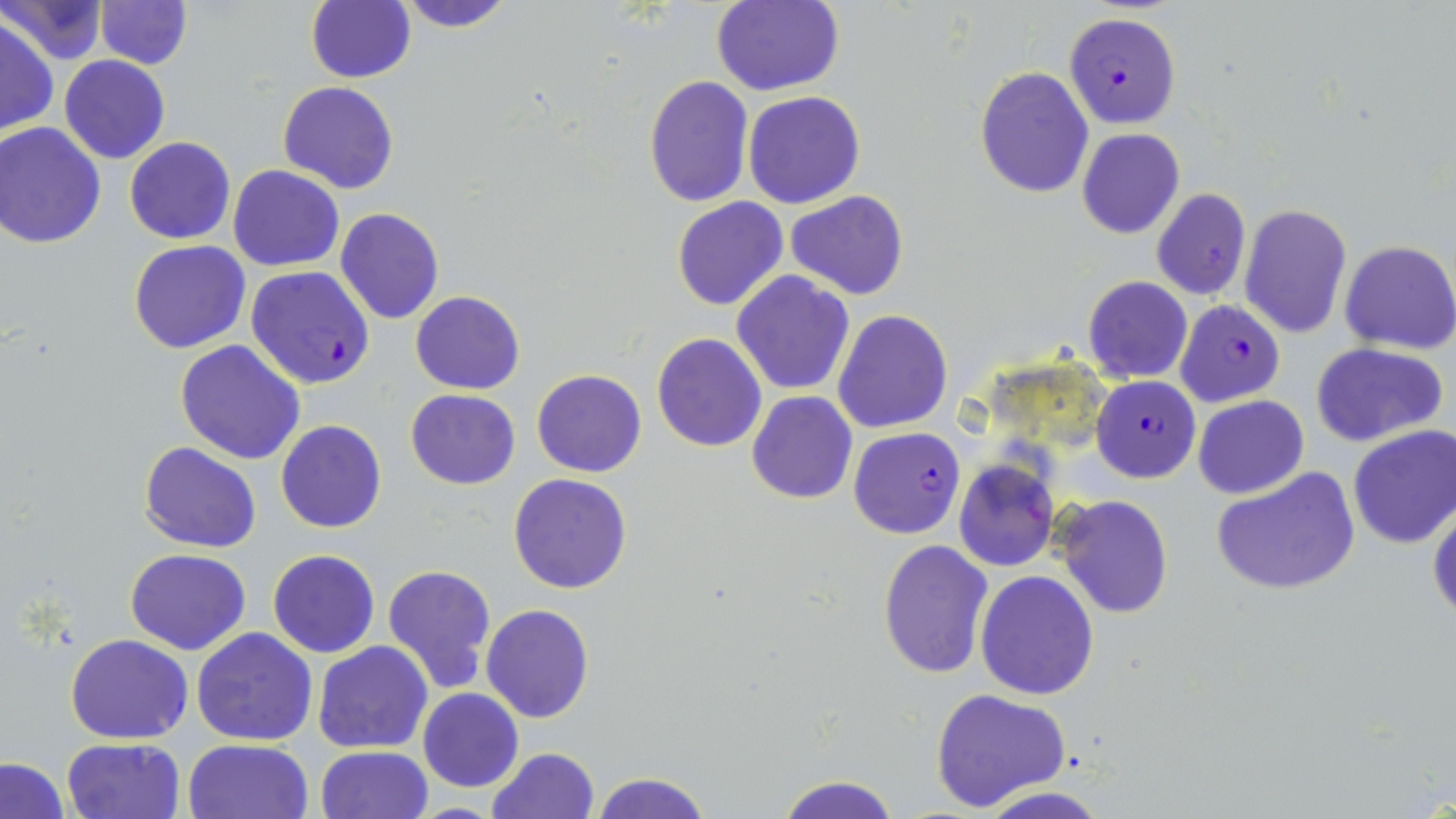

Approximate bounding boxes as [x1, y1, x2, y2] in pixels. Plasmodium falciparum-infected red blood cell locations: [1064, 12, 1181, 128], [246, 266, 374, 389], [1175, 300, 1285, 406], [1091, 375, 1201, 483], [849, 428, 964, 539]. Uninfected red blood cell locations: [0, 0, 105, 64], [95, 0, 192, 70], [305, 0, 415, 85], [394, 0, 514, 32], [711, 1, 843, 96], [0, 17, 57, 136], [60, 55, 170, 164], [974, 66, 1093, 198], [643, 76, 754, 208], [277, 81, 400, 195], [743, 91, 867, 209], [0, 123, 106, 249], [1077, 129, 1185, 240], [125, 136, 235, 243], [229, 164, 344, 271], [1151, 188, 1252, 301], [785, 191, 910, 300], [672, 197, 789, 312], [1240, 204, 1353, 338], [335, 208, 444, 326], [129, 240, 251, 353], [1338, 240, 1456, 354], [733, 271, 855, 394], [1083, 276, 1193, 384], [410, 291, 525, 394], [833, 310, 953, 433], [652, 332, 768, 453], [176, 338, 306, 463], [1311, 342, 1447, 447], [532, 370, 647, 477], [403, 388, 520, 490], [747, 393, 857, 504], [1193, 394, 1308, 499], [276, 420, 387, 533], [1348, 425, 1456, 550], [139, 441, 261, 554], [954, 461, 1058, 572], [1211, 467, 1360, 596], [508, 473, 633, 594], [1054, 494, 1172, 619], [1428, 499, 1456, 622], [878, 540, 993, 678], [125, 548, 251, 655], [267, 550, 380, 658], [382, 563, 496, 693], [976, 570, 1100, 700], [481, 604, 595, 723], [191, 628, 318, 745], [66, 634, 194, 744], [312, 640, 434, 753], [418, 688, 525, 793], [932, 688, 1071, 812], [61, 737, 184, 819], [182, 738, 314, 819], [315, 745, 433, 819], [486, 747, 599, 819], [2, 758, 69, 818], [590, 770, 710, 819], [774, 774, 903, 819], [974, 786, 1112, 819]. Slide-level diagnosis: Plasmodium falciparum. Image is 1456×819 pixels. May-Grünwald-Giemsa-stained preparation. One field of a larger specimen. Captured at 1000x magnification. Light microscopy. Thin blood film.